Assess the morphology of the red blood cells.
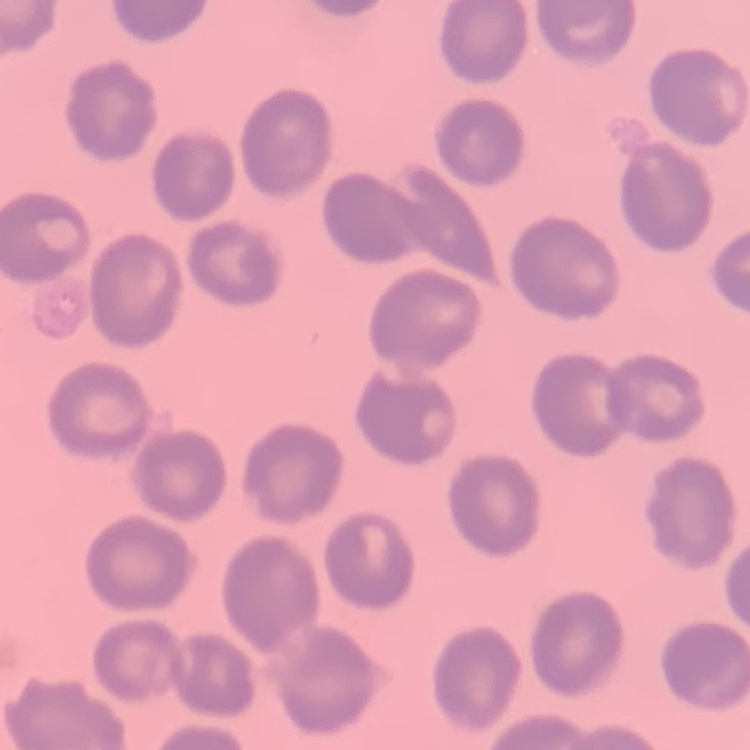

No rouleaux formation.

One tile cut from a larger photomicrograph. Stained with either Field's or Giemsa. Thin peripheral smear.